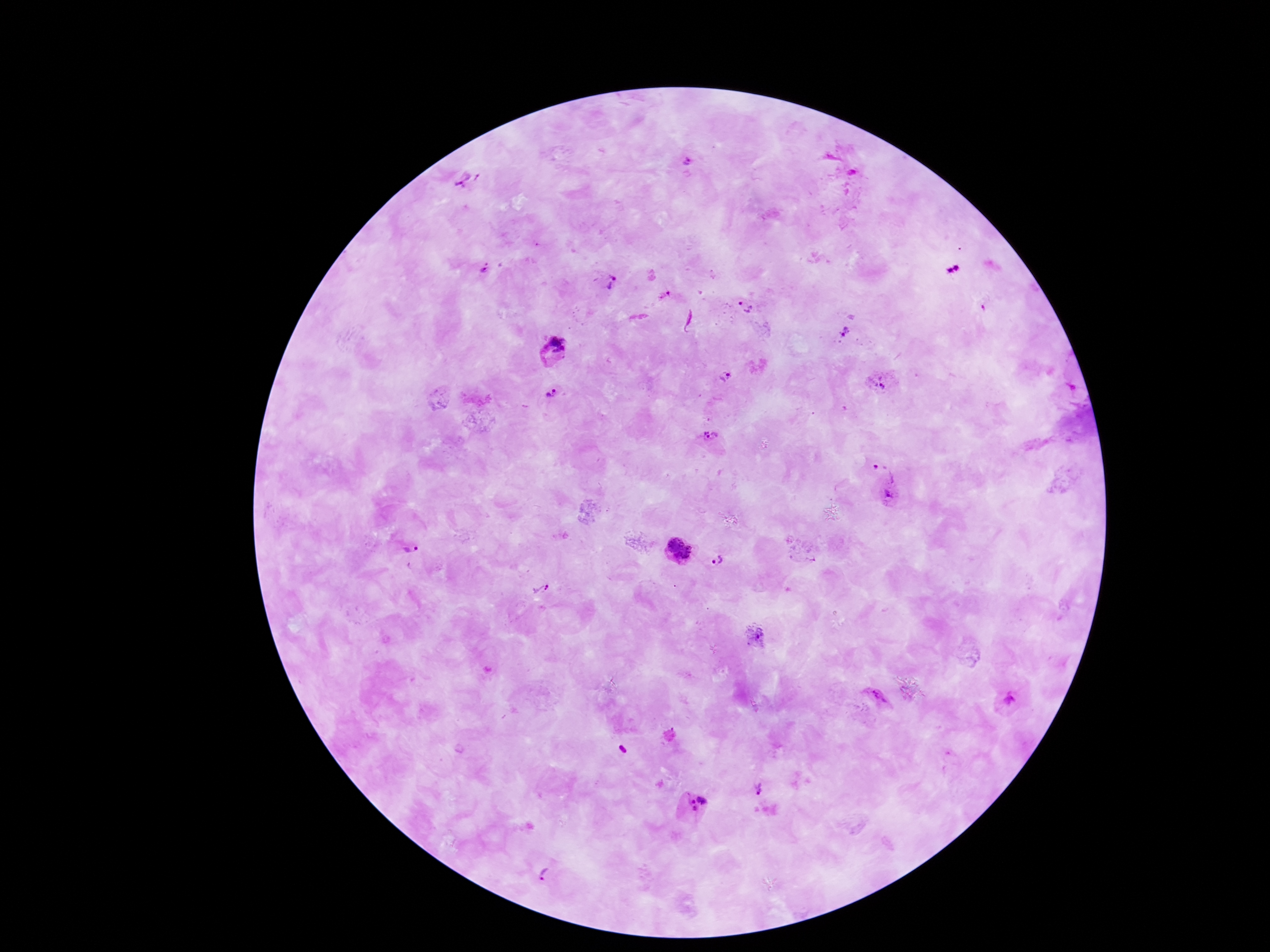
Approximate centers as [x, y] in pixels.
Summary:
  - Plasmodium parasite locations: [686, 162], [468, 179], [485, 269], [608, 285], [666, 301], [744, 308], [845, 331], [552, 352], [727, 377], [879, 382], [555, 395], [714, 438], [886, 471], [889, 497], [408, 549], [679, 551], [718, 563], [541, 591], [756, 636], [878, 698], [1008, 699], [624, 751], [757, 789], [694, 803], [547, 876]
  - Preparation: thick blood film
  - Capture: smartphone camera through the microscope eyepiece
  - Field of view: single
  - Stain: Giemsa
  - Patient malaria status: positive
  - Image size: 1270×952 pixels
  - Magnification: 100x